Classify this cell by malaria status.
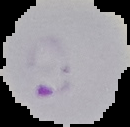
It is parasitized.

From a thin blood film. The area outside the segmented cell region is set to black. Image is 130×127 pixels.